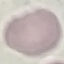
Summary:
  - Result: negative for malaria parasites
  - Preparation: thin smear
  - Image type: automatically extracted cell patch, resized to 64 × 64 pixels
  - Stain: Giemsa
  - Capture: smartphone camera at the microscope eyepiece